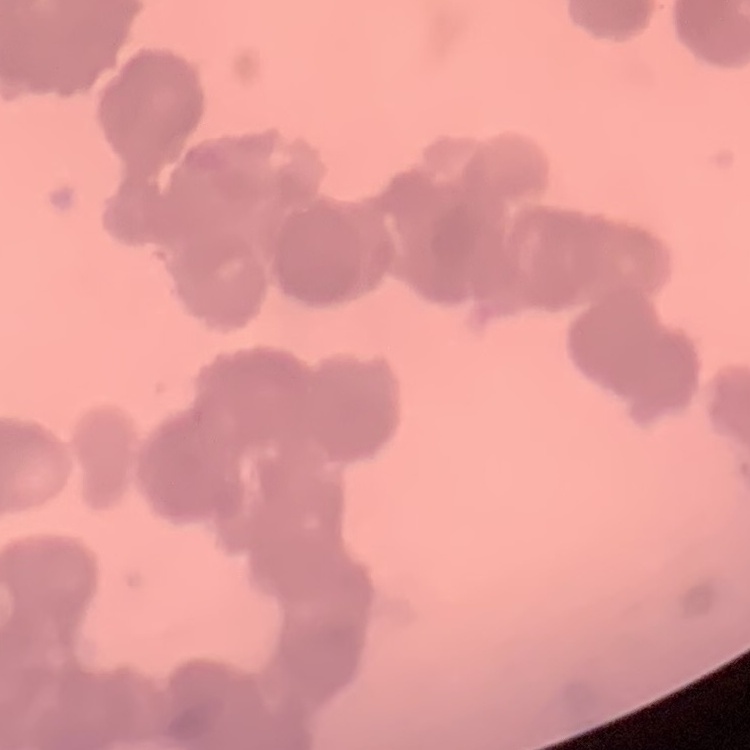
erythrocyte morphology = rouleaux formation
stain = Field's or Giemsa
image type = square crop of a larger photomicrograph
preparation = thin peripheral smear